Give the position of every Plasmodium parasite visible.
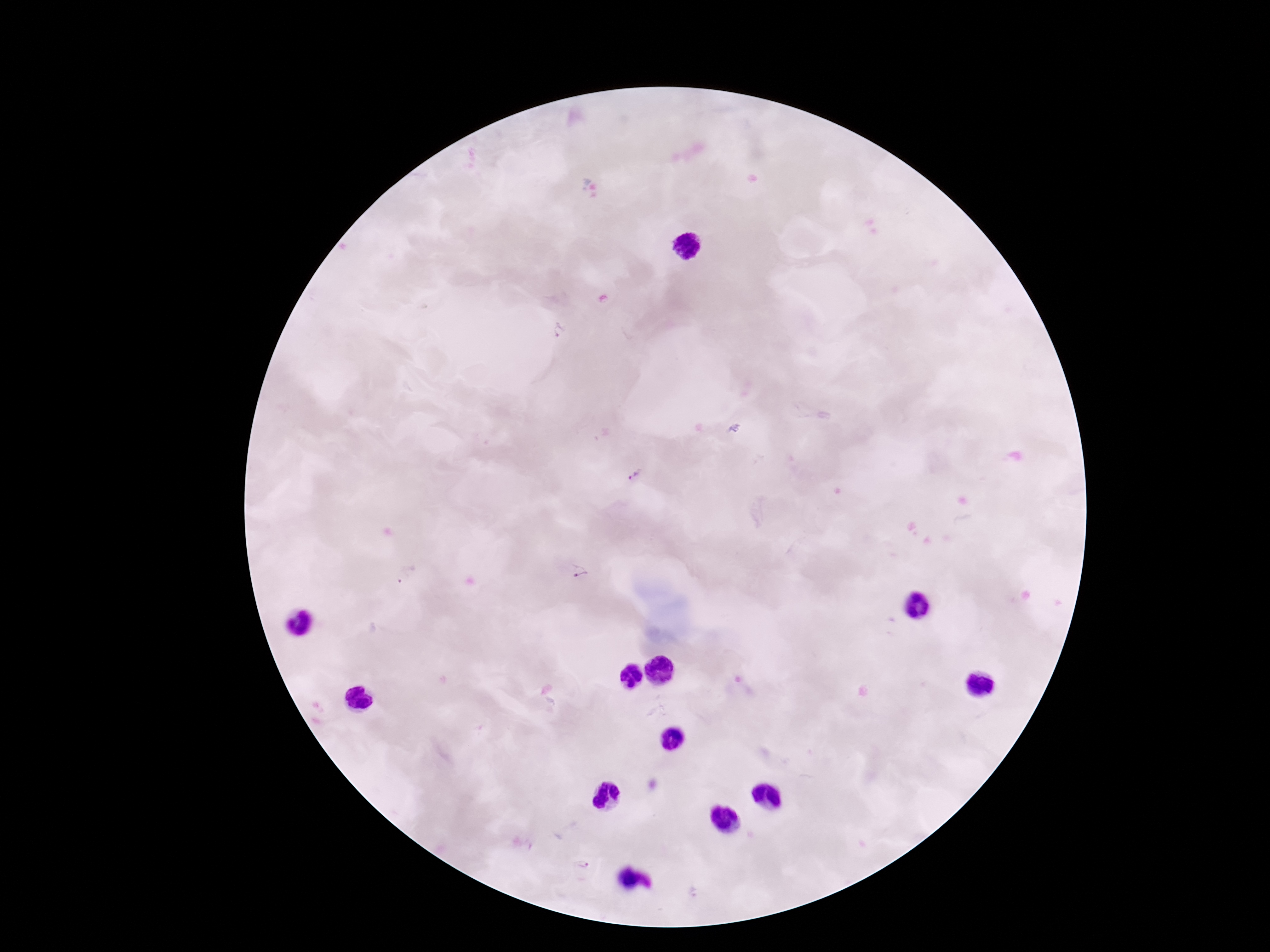
Approximate centers as {x, y} in pixels.
Plasmodium parasites: {559, 331}, {734, 428}, {634, 476}, {579, 573}, {405, 577}, {582, 865}.

{
  "capture": "smartphone camera through the microscope eyepiece",
  "magnification": "100x",
  "stain": "Giemsa",
  "field_of_view": "one from this slide",
  "image_size": "1270×952 pixels",
  "preparation": "thick blood smear",
  "patient_malaria_status": "infected"
}